Identify the preparation type.
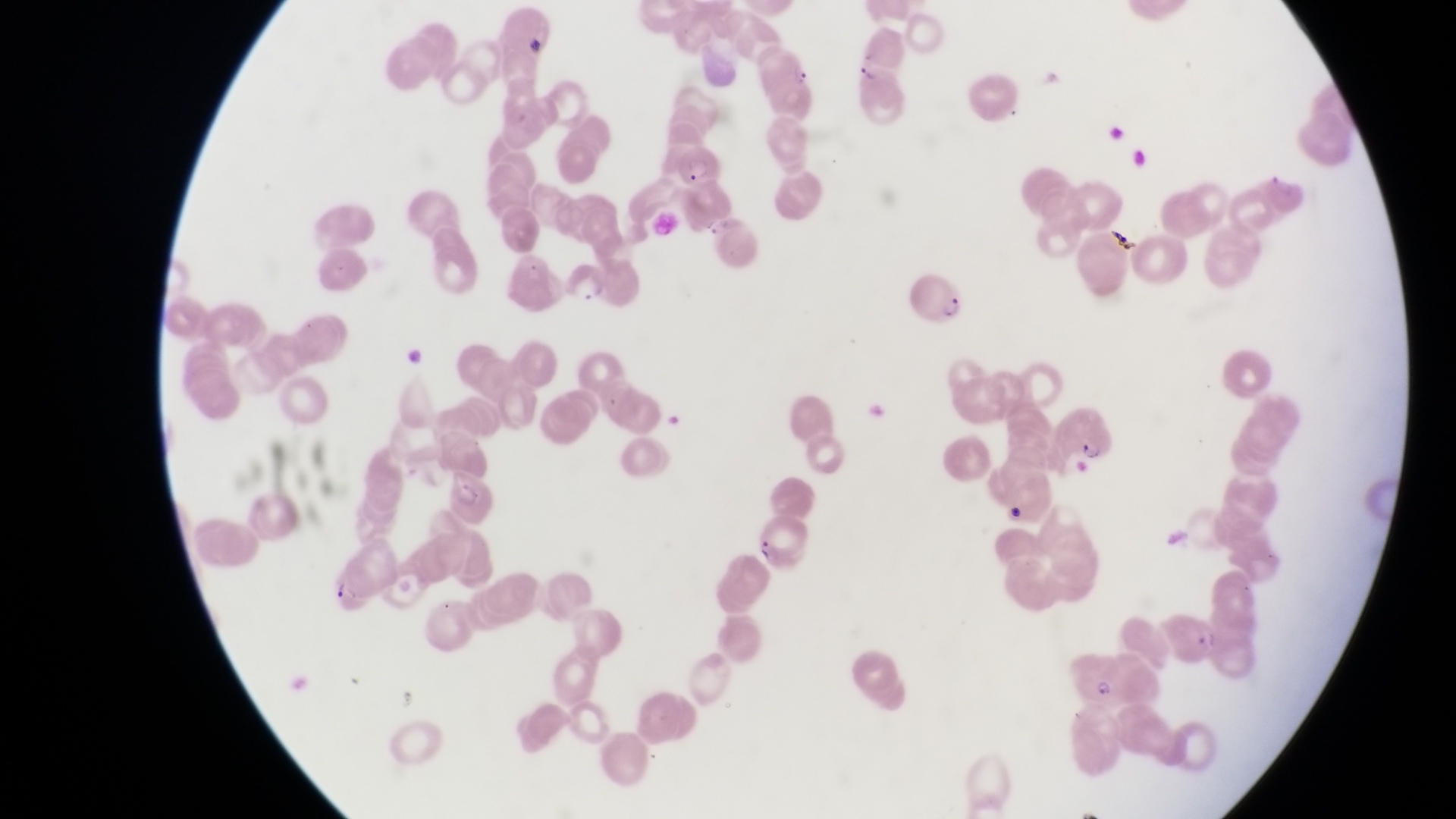
This is a thin smear.

Approximate bounding boxes as left top right bottom in pixels. Parasitised red blood cell locations: 666 127 725 187; 568 258 624 311; 907 261 970 332; 1059 391 1119 464; 1076 644 1125 705. Captured by a smartphone held over the eyepiece of an Olympus CX-23 microscope. Single field of view. Collected in Uganda. Magnification of 1000x. Image is 1456×819 pixels.